Point out every Plasmodium parasite and every leukocyte.
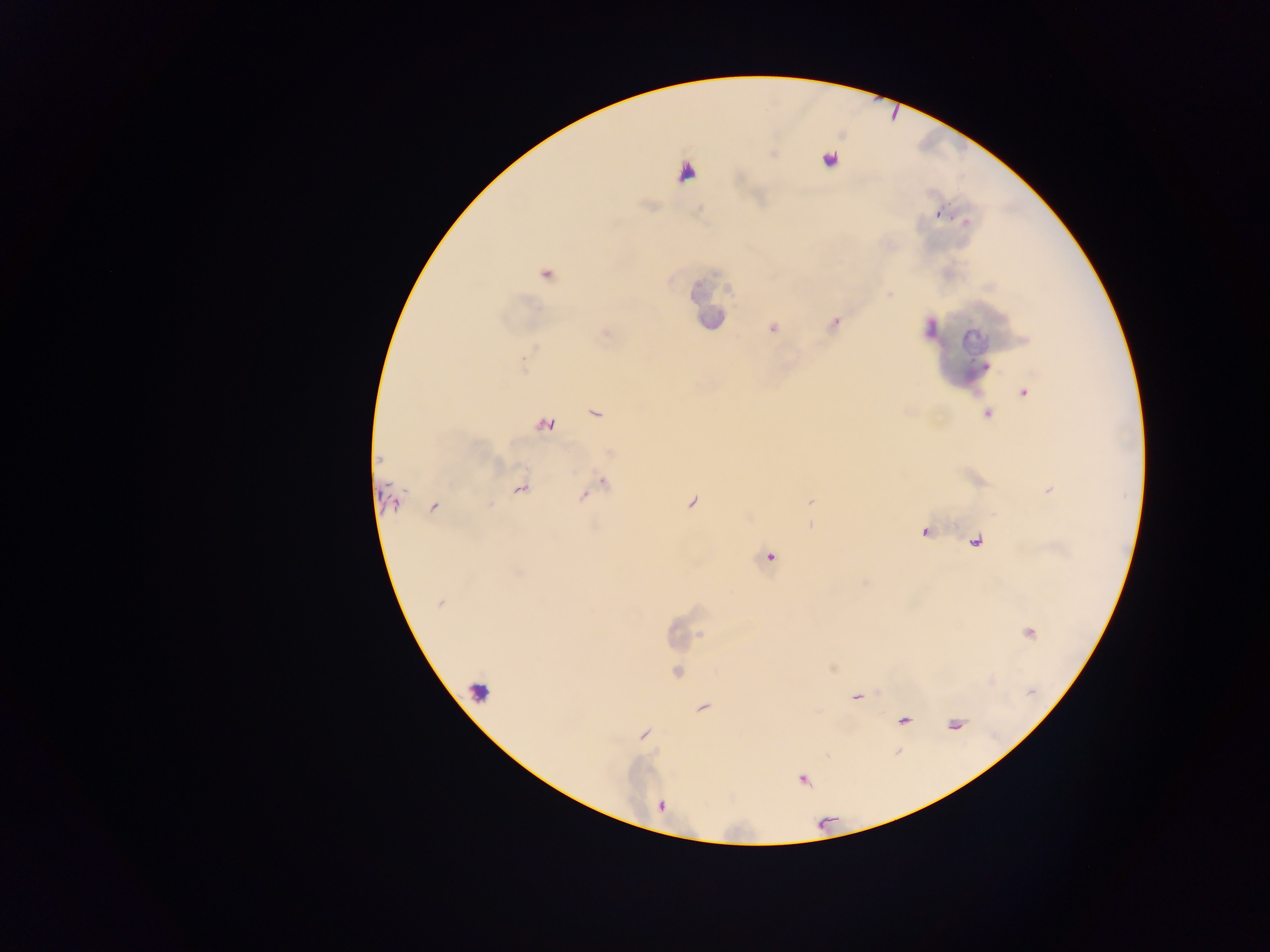
Approximate centers as {x, y} in pixels.
Plasmodium parasites: {828, 160}, {939, 214}, {966, 221}, {546, 275}, {773, 328}, {985, 367}, {1025, 392}, {594, 414}, {987, 415}, {545, 424}, {379, 460}, {603, 483}, {521, 489}, {584, 496}, {393, 501}, {489, 505}, {432, 507}, {770, 557}, {439, 603}, {677, 672}, {703, 708}, {803, 780}.
Leukocytes: {711, 301}, {976, 339}.

Thick blood smear. Photographed through a microscope with a mobile-phone camera. Collected in Ghana. Single field of view. Image is 1270×952 pixels.